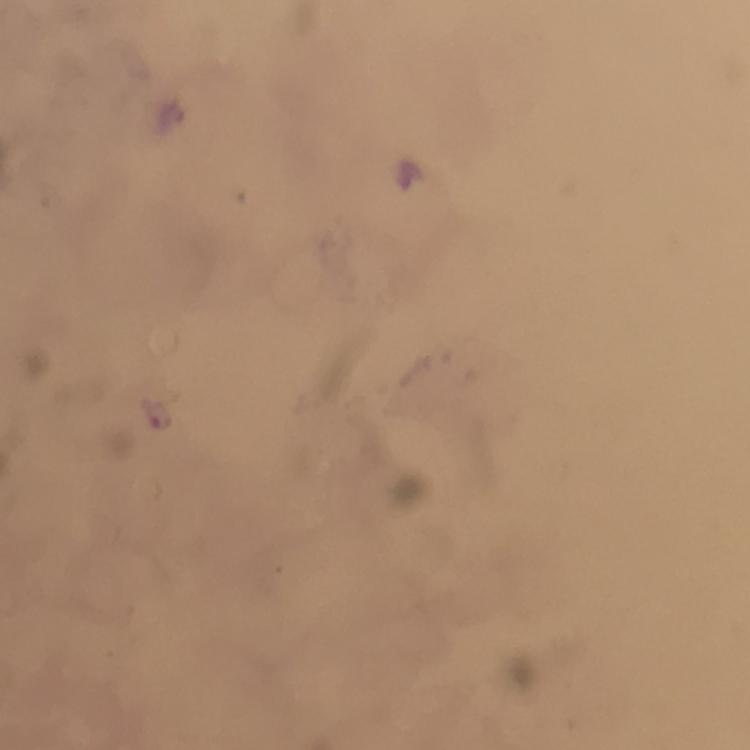

Approximate object centers, in pixels from the top-left corner.
Summary:
  - Plasmodium parasite locations: (x=160, y=414)
  - Cropped from: a single field of view
  - Stain: Giemsa
  - Capture: smartphone camera through the microscope
  - Preparation: thick smear
  - Magnification: 100x
  - Image size: 750×750 pixels
  - Context: from a diagnostic examination for malaria
  - Immersion oil: applied